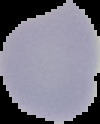
Summary:
  - Image type: cell region segmented out of the field of view; surrounding area masked to black
  - Preparation: thin blood smear
  - Image size: 100×124 pixels
  - Malaria status: uninfected